Identify the parasite.
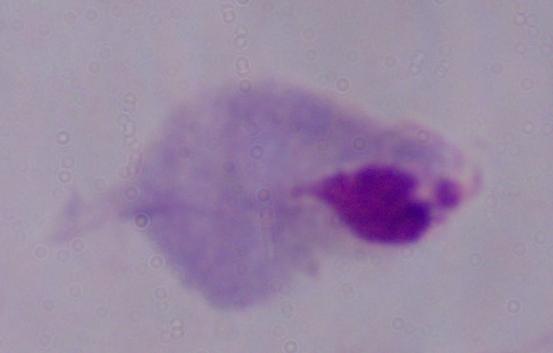

A trichomonad.

Micrograph. 1000x magnification.